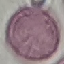
Summary:
  - Result: negative for malaria parasites
  - Image type: cell patch, automatically extracted from a larger field of view and resized to 64 × 64 pixels
  - Capture: smartphone through the microscope eyepiece
  - Preparation: thin blood film
  - Stain: Giemsa